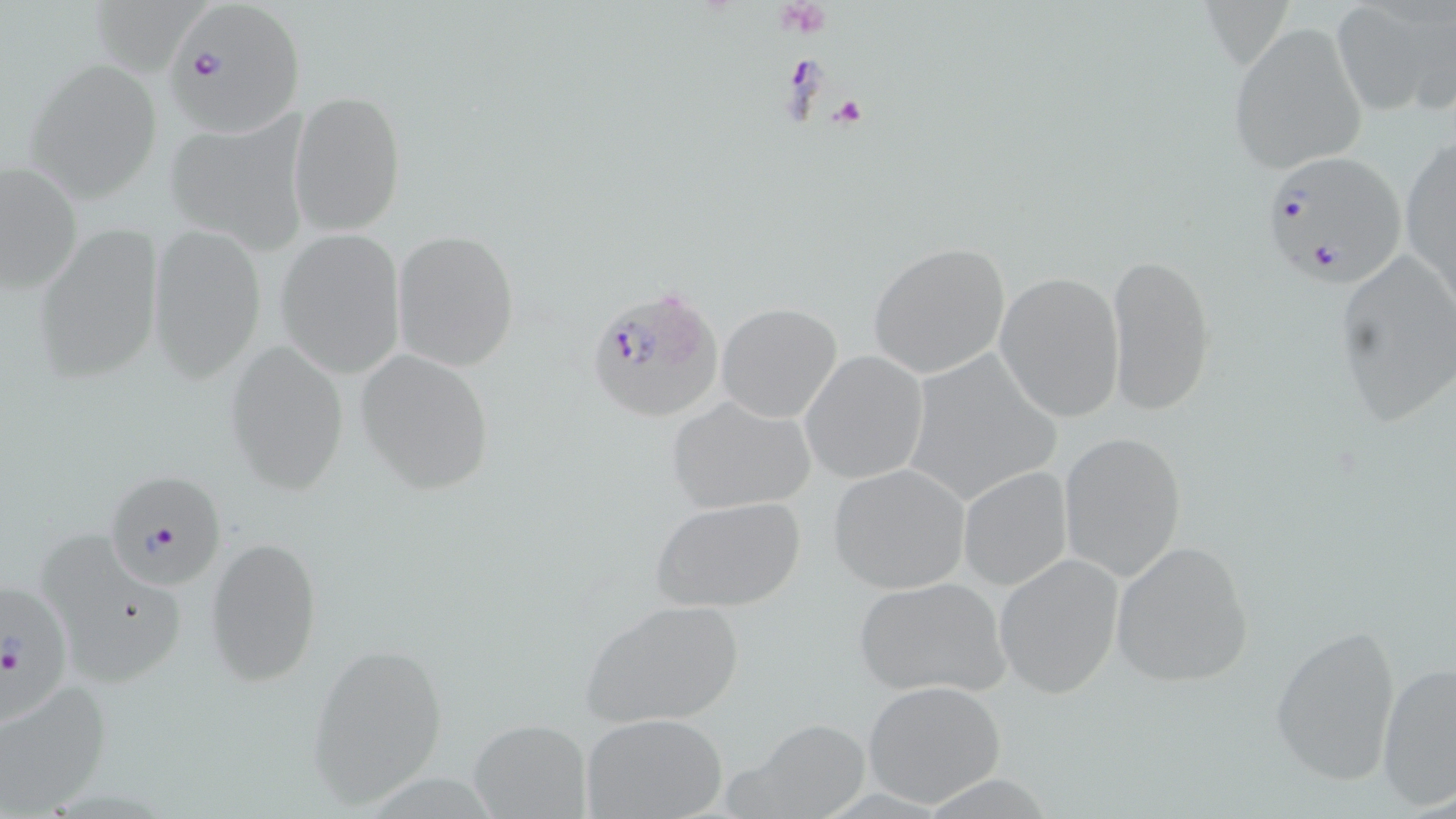

Approximate bounding boxes as (x1,y1)-(x2,y2) corner pairs in pixels. Uninfected red blood cell locations: (1329,0)-(1452,119), (1228,21)-(1368,175), (25,59)-(163,202), (290,90)-(406,236), (163,113)-(307,252), (1400,131)-(1456,313), (0,159)-(84,298), (33,221)-(164,384), (147,221)-(265,383), (275,227)-(406,379), (392,229)-(519,372), (867,241)-(1010,379), (1104,249)-(1214,417), (1332,252)-(1454,432), (995,270)-(1128,422), (716,303)-(843,423), (224,340)-(350,495), (899,348)-(1065,508), (355,350)-(494,494), (799,350)-(929,485), (665,395)-(819,514), (1057,430)-(1187,583), (828,464)-(969,594), (958,467)-(1071,590), (650,494)-(809,613), (206,536)-(323,688), (39,538)-(193,691), (1108,539)-(1254,688), (994,552)-(1125,698), (850,576)-(1013,699), (579,598)-(746,730), (1268,623)-(1402,787), (305,641)-(448,805), (1378,660)-(1456,810), (0,678)-(114,811), (862,680)-(1006,807), (579,712)-(730,819), (466,719)-(592,818), (741,722)-(872,814). Platelet locations: (776,0)-(829,38), (832,96)-(868,127). Plasmodium falciparum-infected red blood cell locations: (166,3)-(304,138), (1258,150)-(1406,290), (584,282)-(723,423), (104,470)-(226,592), (0,576)-(75,727). Slide-level diagnosis: Plasmodium falciparum. 1000x magnification. One field of a larger specimen. Image is 1456×819 pixels. Light microscopy. Thin blood smear. May-Grünwald-Giemsa stain.